Locate every blood parasite and identify its species.
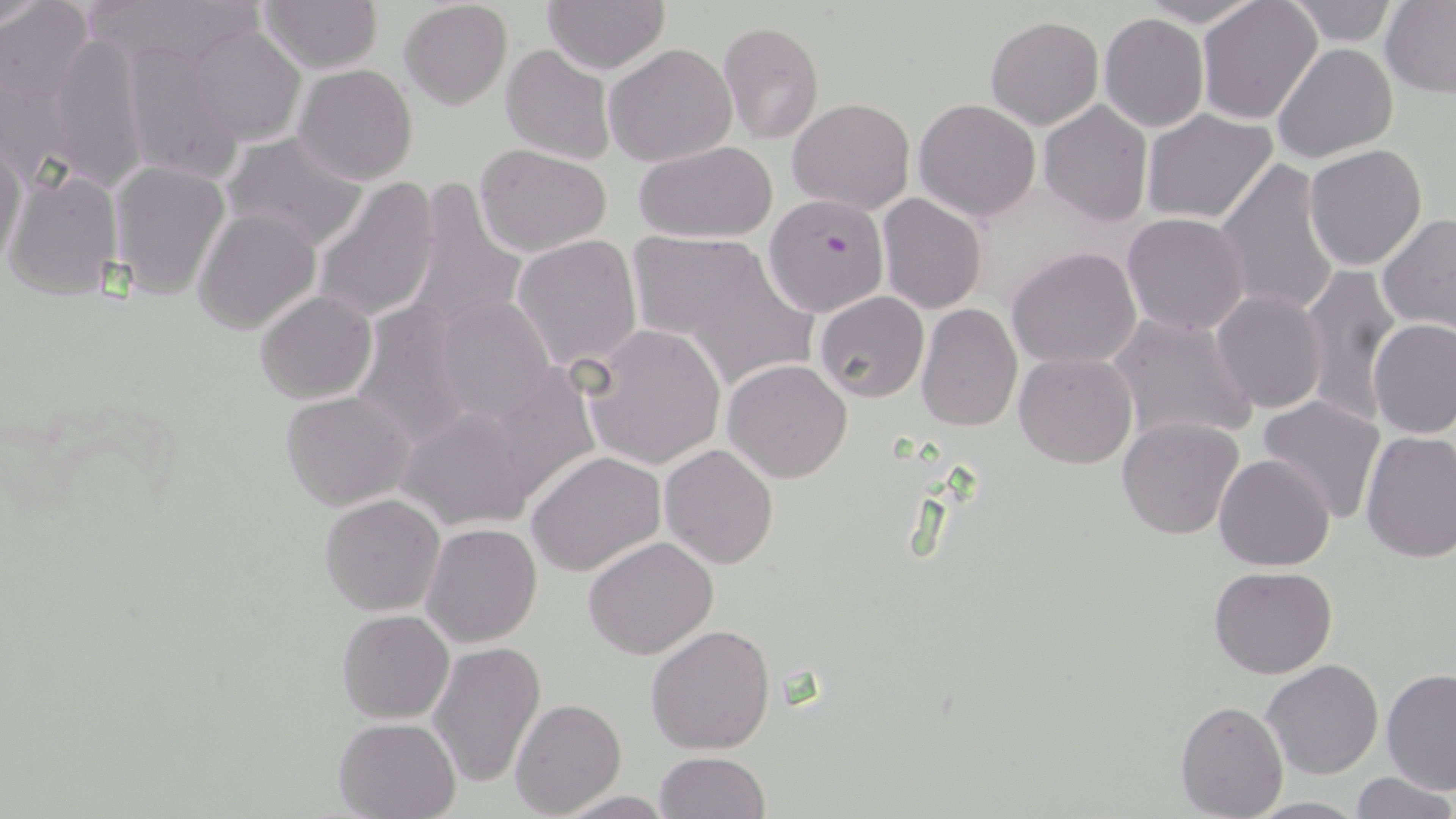
Approximate bounding boxes as (x1, y1, x2, y2) in pixels.
Plasmodium falciparum-infected red blood cells: (762, 192, 891, 318).
No Plasmodium ovale, Plasmodium malariae, Plasmodium vivax, Babesia divergens, or Trypanosoma brucei observed.

slide-level diagnosis = Plasmodium falciparum
magnification = 1000x
modality = light microscopy
stain = May-Grünwald-Giemsa
image size = 1456×819 pixels
uninfected red blood cell locations = approximate bounding boxes as (x1, y1, x2, y2) in pixels: (84, 0, 259, 74), (541, 0, 670, 73), (1134, 0, 1263, 27), (1196, 0, 1324, 126), (0, 1, 57, 37), (1, 1, 94, 112), (259, 1, 383, 73), (398, 1, 513, 110), (1287, 1, 1401, 46), (1380, 1, 1456, 97), (1098, 11, 1210, 133), (986, 16, 1104, 131), (717, 20, 825, 145), (187, 23, 307, 148), (47, 31, 150, 188), (119, 41, 245, 185), (605, 43, 736, 168), (1273, 43, 1398, 164), (500, 45, 615, 164), (293, 63, 419, 185), (789, 98, 915, 214), (912, 98, 1042, 223), (1039, 100, 1153, 227), (1139, 108, 1277, 226), (221, 129, 371, 251), (1, 132, 28, 268), (633, 140, 777, 243), (474, 143, 615, 258), (1304, 144, 1428, 271), (1213, 157, 1340, 320), (107, 159, 232, 301), (4, 169, 124, 302), (311, 176, 439, 326), (405, 179, 527, 331), (876, 193, 989, 314), (192, 205, 321, 337), (1122, 213, 1252, 336), (1378, 214, 1455, 335), (1010, 229, 1250, 353), (627, 232, 769, 340), (511, 234, 644, 373), (1008, 245, 1142, 370), (688, 256, 819, 390), (1300, 261, 1403, 423), (703, 271, 838, 470), (254, 289, 377, 405), (1209, 290, 1328, 412), (813, 292, 929, 404), (434, 293, 558, 425), (349, 299, 475, 450), (916, 302, 1023, 433), (1107, 313, 1258, 447), (1369, 319, 1456, 439), (578, 322, 726, 471), (1013, 351, 1138, 469), (722, 358, 853, 483), (486, 361, 602, 507), (280, 390, 415, 510), (1257, 394, 1386, 524), (396, 407, 534, 531), (1116, 415, 1246, 540), (1360, 431, 1456, 563), (660, 444, 779, 569), (527, 451, 666, 577), (1212, 454, 1335, 572), (320, 494, 445, 616), (420, 523, 542, 647), (583, 536, 719, 660), (1208, 567, 1337, 680), (336, 610, 454, 724), (646, 623, 778, 754), (428, 640, 547, 790), (1260, 660, 1383, 781), (1380, 668, 1456, 794), (1175, 680, 1372, 802), (510, 698, 626, 818), (1175, 699, 1288, 818), (332, 717, 461, 819), (653, 751, 770, 819), (1348, 772, 1455, 819), (1246, 796, 1368, 818)
field of view = single
preparation = thin blood smear